Locate every leukocyte (white blood cell).
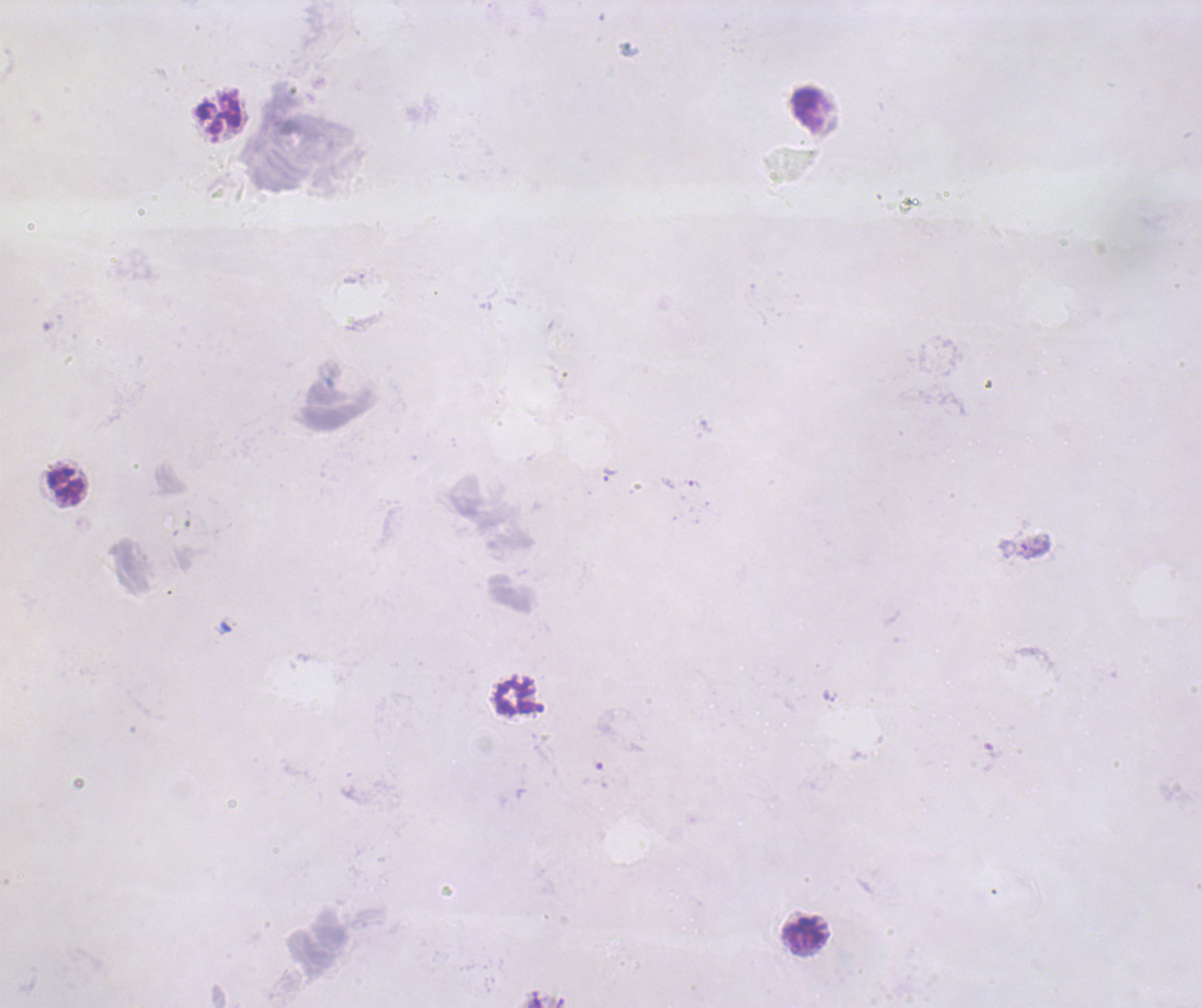

Approximate object centers, in pixels from the top-left corner.
Leukocytes: (x=809, y=109), (x=218, y=114), (x=66, y=484), (x=515, y=697), (x=804, y=935).

Approximate object centers, in pixels from the top-left corner. Trophozoite locations: (x=609, y=475), (x=692, y=484). Romanowsky-stained preparation. Image is 1202×1008 pixels. Previously used in an actual diagnosis. Result: positive for malaria parasites. One field from this slide. Background quality: unsatisfactory. Captured at 100x magnification. Thick blood film. Coloration quality: bad.